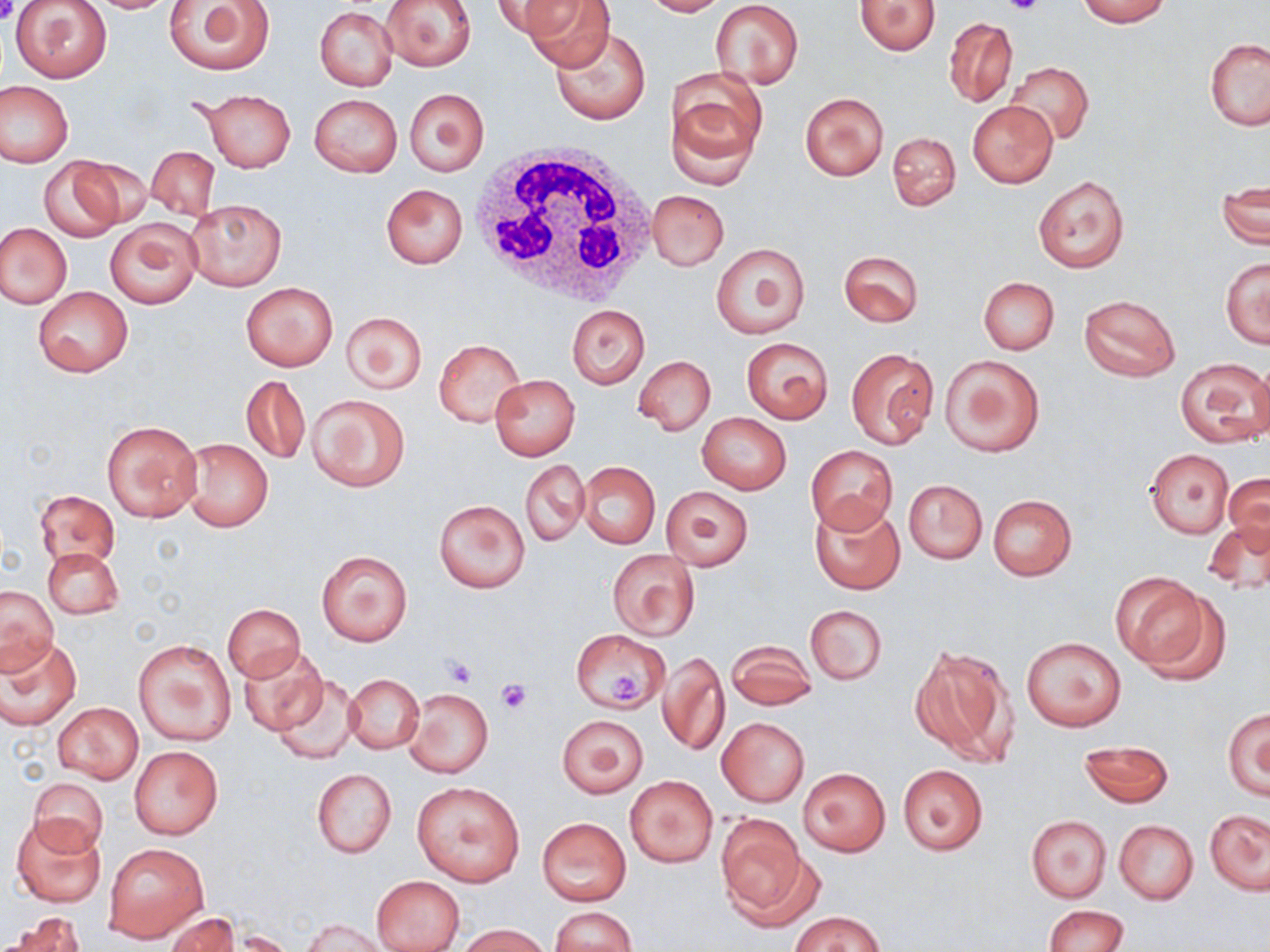
Summary:
  - Coordinate format: approximate bounding boxes as named x1/y1/x2/y2 corners in pixels
  - White blood cell locations: (x1=472, y1=141, x2=660, y2=309)
  - Platelet locations: (x1=1001, y1=0, x2=1046, y2=18), (x1=0, y1=1, x2=21, y2=25), (x1=441, y1=653, x2=479, y2=687), (x1=607, y1=670, x2=646, y2=705), (x1=497, y1=679, x2=527, y2=712)
  - Uninfected red blood cell locations: (x1=164, y1=0, x2=276, y2=75), (x1=382, y1=0, x2=477, y2=69), (x1=489, y1=0, x2=579, y2=37), (x1=521, y1=0, x2=615, y2=68), (x1=642, y1=0, x2=727, y2=17), (x1=1075, y1=0, x2=1170, y2=26), (x1=11, y1=1, x2=111, y2=84), (x1=83, y1=1, x2=183, y2=13), (x1=710, y1=1, x2=804, y2=87), (x1=855, y1=1, x2=940, y2=55), (x1=315, y1=7, x2=397, y2=91), (x1=944, y1=18, x2=1017, y2=108), (x1=549, y1=26, x2=651, y2=126), (x1=1204, y1=39, x2=1270, y2=131), (x1=1005, y1=61, x2=1094, y2=145), (x1=665, y1=68, x2=768, y2=177), (x1=0, y1=81, x2=73, y2=166), (x1=404, y1=87, x2=489, y2=176), (x1=196, y1=88, x2=296, y2=172), (x1=799, y1=91, x2=890, y2=181), (x1=308, y1=93, x2=403, y2=177), (x1=968, y1=101, x2=1058, y2=187), (x1=888, y1=132, x2=960, y2=211), (x1=146, y1=145, x2=220, y2=221), (x1=69, y1=155, x2=156, y2=229), (x1=36, y1=156, x2=127, y2=243), (x1=1032, y1=176, x2=1130, y2=273), (x1=380, y1=184, x2=468, y2=267), (x1=1216, y1=184, x2=1268, y2=248), (x1=647, y1=189, x2=730, y2=270), (x1=185, y1=198, x2=285, y2=292), (x1=104, y1=218, x2=202, y2=309), (x1=1, y1=224, x2=71, y2=308), (x1=711, y1=243, x2=811, y2=339), (x1=838, y1=250, x2=924, y2=327), (x1=1221, y1=257, x2=1269, y2=349), (x1=979, y1=277, x2=1059, y2=355), (x1=241, y1=281, x2=338, y2=371), (x1=34, y1=288, x2=132, y2=378), (x1=1078, y1=294, x2=1181, y2=382), (x1=566, y1=305, x2=649, y2=388), (x1=342, y1=310, x2=427, y2=394), (x1=741, y1=337, x2=832, y2=422), (x1=433, y1=338, x2=525, y2=427), (x1=845, y1=348, x2=938, y2=448), (x1=940, y1=353, x2=1045, y2=457), (x1=633, y1=355, x2=715, y2=435), (x1=1174, y1=359, x2=1268, y2=447), (x1=1248, y1=360, x2=1270, y2=444), (x1=241, y1=374, x2=311, y2=464), (x1=490, y1=374, x2=580, y2=460), (x1=307, y1=393, x2=410, y2=491), (x1=697, y1=412, x2=791, y2=494), (x1=101, y1=420, x2=202, y2=522), (x1=180, y1=437, x2=273, y2=533), (x1=806, y1=444, x2=898, y2=533), (x1=1145, y1=449, x2=1234, y2=537), (x1=520, y1=460, x2=589, y2=546), (x1=577, y1=462, x2=660, y2=549), (x1=1222, y1=472, x2=1270, y2=551), (x1=904, y1=479, x2=987, y2=564), (x1=660, y1=485, x2=755, y2=570), (x1=35, y1=490, x2=119, y2=568), (x1=987, y1=493, x2=1077, y2=580), (x1=433, y1=498, x2=530, y2=593), (x1=811, y1=498, x2=904, y2=595), (x1=1202, y1=519, x2=1270, y2=594), (x1=44, y1=547, x2=123, y2=620), (x1=608, y1=548, x2=700, y2=641), (x1=316, y1=550, x2=413, y2=646), (x1=1114, y1=575, x2=1224, y2=680), (x1=0, y1=585, x2=58, y2=672), (x1=223, y1=603, x2=306, y2=682), (x1=805, y1=604, x2=887, y2=684), (x1=573, y1=628, x2=671, y2=713), (x1=0, y1=633, x2=82, y2=729), (x1=1019, y1=636, x2=1125, y2=732), (x1=133, y1=638, x2=236, y2=749), (x1=725, y1=639, x2=817, y2=709), (x1=911, y1=644, x2=1016, y2=766), (x1=237, y1=645, x2=329, y2=736), (x1=659, y1=650, x2=729, y2=757), (x1=344, y1=673, x2=423, y2=754), (x1=271, y1=676, x2=362, y2=765), (x1=405, y1=688, x2=493, y2=777), (x1=54, y1=703, x2=142, y2=782), (x1=1223, y1=708, x2=1270, y2=800), (x1=556, y1=714, x2=648, y2=798), (x1=716, y1=717, x2=809, y2=808), (x1=1079, y1=740, x2=1173, y2=807), (x1=130, y1=745, x2=223, y2=839), (x1=897, y1=764, x2=988, y2=855), (x1=799, y1=767, x2=890, y2=856), (x1=312, y1=768, x2=396, y2=858), (x1=626, y1=775, x2=718, y2=866), (x1=28, y1=776, x2=109, y2=854), (x1=411, y1=781, x2=525, y2=886), (x1=1205, y1=810, x2=1269, y2=894), (x1=716, y1=813, x2=811, y2=918), (x1=12, y1=814, x2=106, y2=906), (x1=1026, y1=815, x2=1110, y2=901), (x1=537, y1=817, x2=631, y2=905), (x1=1113, y1=819, x2=1198, y2=903), (x1=103, y1=841, x2=207, y2=943), (x1=371, y1=875, x2=465, y2=952), (x1=1042, y1=905, x2=1129, y2=951), (x1=551, y1=907, x2=637, y2=952), (x1=794, y1=911, x2=882, y2=952), (x1=8, y1=912, x2=86, y2=952), (x1=165, y1=912, x2=239, y2=952), (x1=303, y1=919, x2=390, y2=952), (x1=459, y1=924, x2=548, y2=952)
  - Slide-level diagnosis: no evidence of blood parasites
  - Stain: May-Grünwald-Giemsa
  - Magnification: 1000x
  - Field of view: single
  - Modality: optical microscopy
  - Image size: 1270×952 pixels
  - Preparation: thin blood film